State which parasite is depicted.
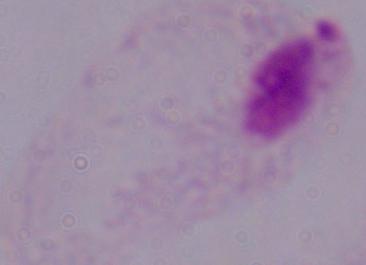
This is a trichomonad.

magnification = 1000x
modality = micrograph